Point out each leukocyte.
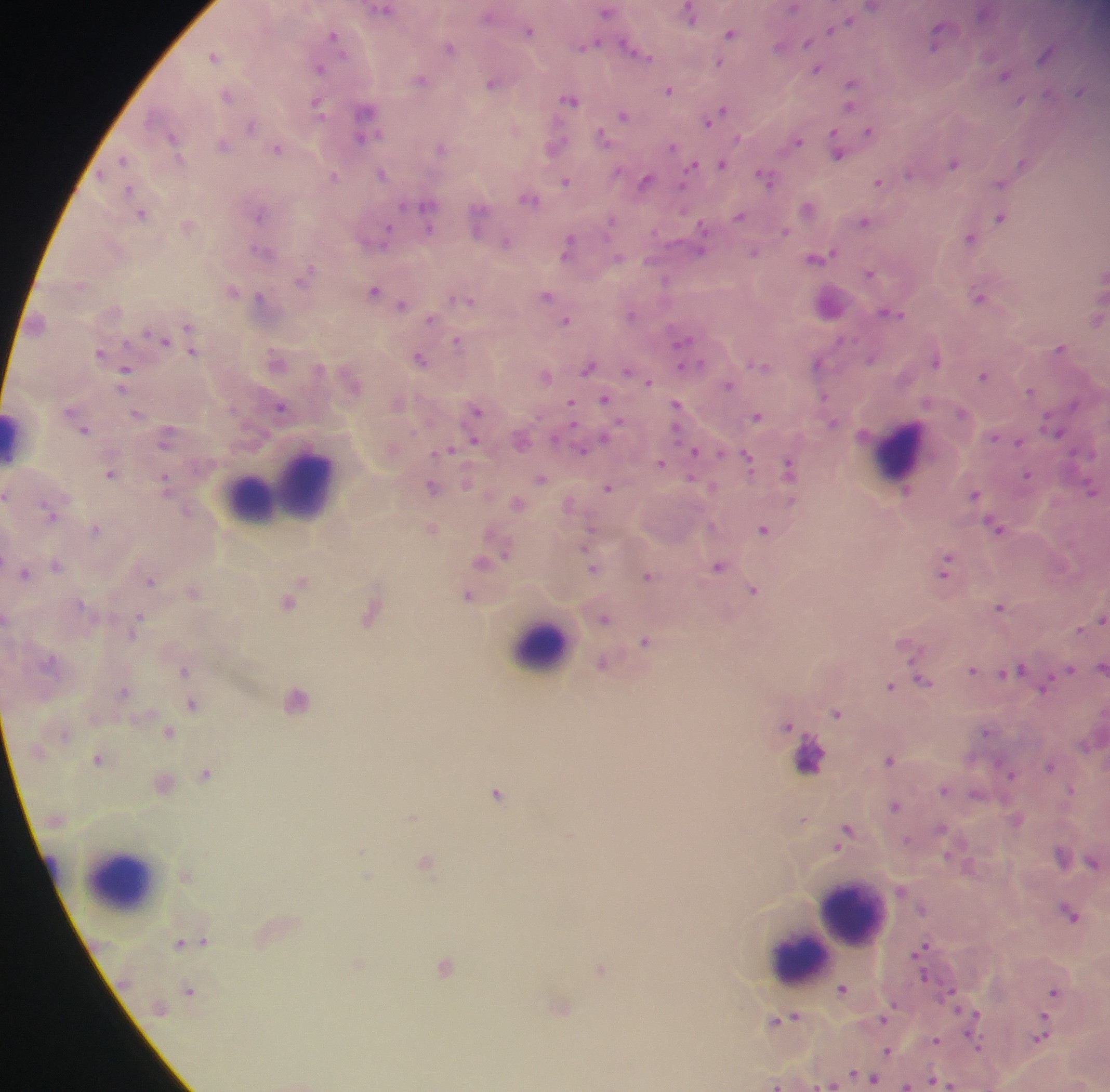
Approximate centers as x y in pixels.
Leukocytes: 14 437; 901 452; 284 486; 246 498; 542 647; 810 756; 52 866; 120 879; 852 914; 799 957.

Plasmodium parasite locations: 382 8; 607 10; 690 13; 849 19; 839 25; 530 29; 832 29; 731 33; 335 34; 938 34; 807 41; 589 44; 780 45; 450 47; 633 48; 1047 53; 214 55; 720 62; 321 67; 817 68; 1005 74; 422 79; 494 82; 852 84; 669 90; 1080 91; 228 95; 572 99; 1021 101; 318 104; 623 114; 717 114; 366 116; 252 125; 516 128; 869 131; 364 132; 173 136; 604 137; 797 140; 224 145; 555 145; 441 147; 674 147; 278 148; 838 151; 124 159; 1023 161; 722 163; 954 163; 694 164; 383 173; 910 173; 335 176; 767 177; 566 180; 646 181; 879 181; 1001 184; 130 189; 529 196; 428 205; 808 208; 142 212; 260 213; 740 216; 1001 217; 479 220; 612 220; 864 221; 189 224; 785 231; 385 234; 970 237; 506 241; 570 245; 700 246; 262 250; 753 252; 821 255; 871 272; 305 276; 666 280; 232 290; 375 291; 547 295; 980 296; 261 297; 463 298; 829 303; 402 305; 891 311; 632 314; 1097 318; 432 319; 566 320; 189 328; 157 336; 458 341; 683 343; 1061 348; 192 351; 101 352; 421 358; 684 359; 278 361; 936 361; 819 363; 760 364; 589 366; 126 368; 631 373; 546 375; 984 375; 647 380; 730 384; 1030 390; 606 399; 398 403; 677 404; 571 405; 282 406; 476 410; 138 413; 757 416; 75 418; 1054 428; 85 429; 168 435; 995 436; 522 439; 474 440; 1017 441; 584 448; 448 450; 696 451; 748 459; 662 463; 789 467; 111 474; 1027 474; 541 478; 166 482; 608 487; 432 488; 1092 490; 975 493; 7 494; 518 502; 570 504; 52 514; 998 527; 432 528; 765 528; 96 529; 490 554; 484 561; 57 565; 719 565; 946 566; 594 567; 25 573; 649 575; 151 579; 301 580; 193 590; 754 590; 295 591; 470 596; 288 601; 1001 607; 371 613; 605 617; 1101 620; 136 625; 646 641; 603 662; 1101 668; 1069 669; 185 670; 973 670; 1011 670; 922 680; 1045 685; 891 686; 124 691; 297 698; 192 703; 837 713; 788 724; 988 731; 169 732; 99 759; 890 759; 1050 765; 1010 771; 206 774; 163 781; 944 789; 1072 790; 498 793; 896 806; 413 817; 804 819; 1016 819; 847 832; 1063 854; 427 862; 1093 862; 185 876; 1071 913; 200 942; 183 944; 923 950; 445 966; 601 970; 843 989; 190 990; 1054 992; 561 1006; 974 1016; 784 1018; 885 1019; 1042 1036; 976 1040; 936 1041; 888 1052; 867 1078; 940 1081; 777 1085; 907 1085. Collected in Ghana. Mobile-phone photograph taken through the microscope. Image is 1110×1092 pixels. Thick blood smear. Single field of view.